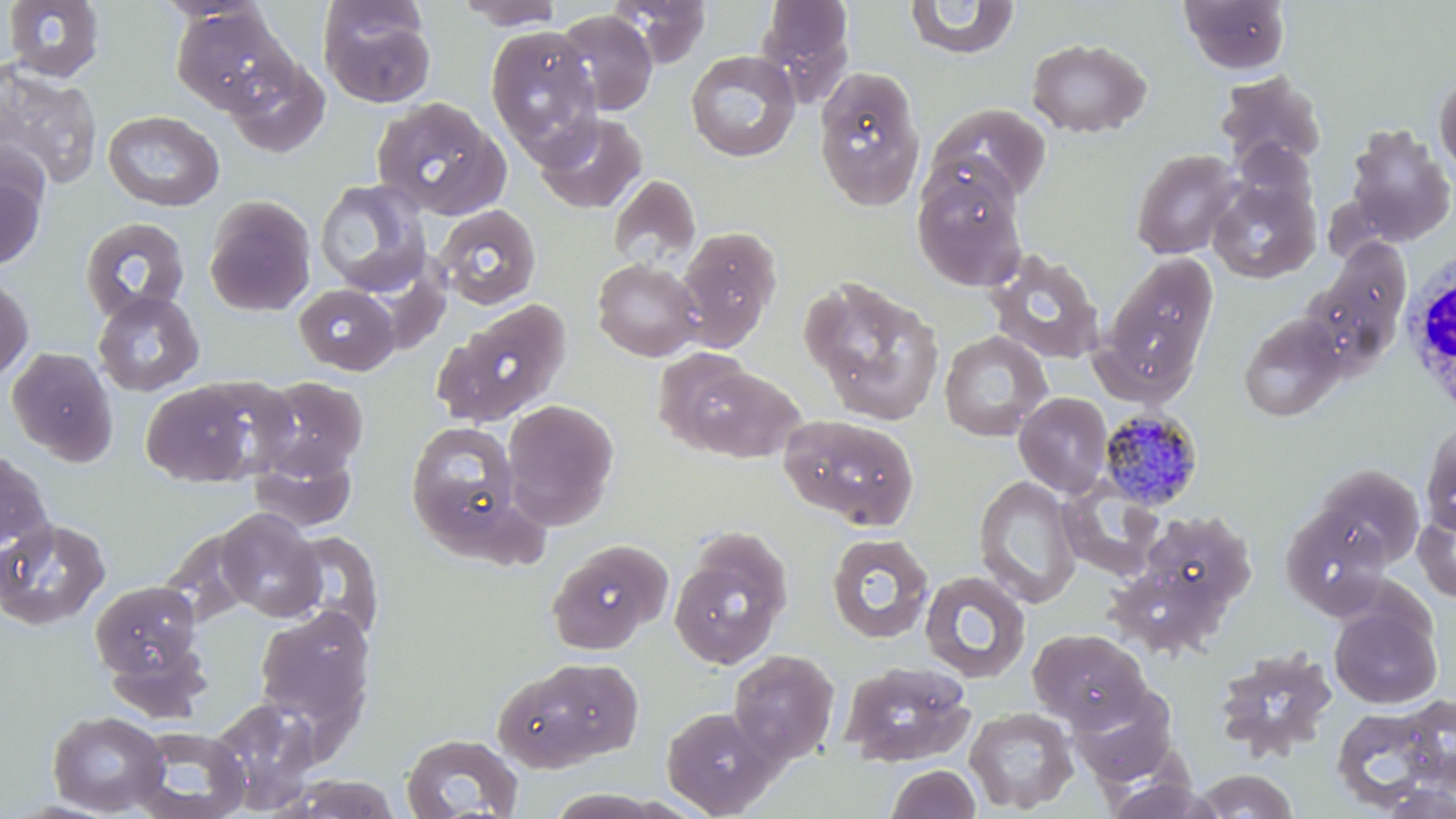
slide-level diagnosis = Plasmodium malariae
stain = May-Grünwald-Giemsa
uninfected red blood cell locations = approximate bounding boxes as named x1/y1/x2/y2 corners in pixels: (x1=2, y1=0, x2=106, y2=83), (x1=451, y1=0, x2=567, y2=29), (x1=606, y1=0, x2=712, y2=68), (x1=755, y1=0, x2=854, y2=90), (x1=1178, y1=0, x2=1292, y2=76), (x1=904, y1=1, x2=1020, y2=59), (x1=317, y1=2, x2=437, y2=109), (x1=170, y1=5, x2=298, y2=117), (x1=555, y1=10, x2=659, y2=116), (x1=484, y1=25, x2=602, y2=156), (x1=1026, y1=37, x2=1151, y2=138), (x1=685, y1=50, x2=801, y2=163), (x1=222, y1=52, x2=329, y2=159), (x1=0, y1=58, x2=103, y2=193), (x1=814, y1=67, x2=926, y2=211), (x1=1434, y1=68, x2=1456, y2=179), (x1=1215, y1=71, x2=1327, y2=172), (x1=371, y1=97, x2=511, y2=219), (x1=928, y1=103, x2=1051, y2=204), (x1=102, y1=110, x2=225, y2=211), (x1=534, y1=111, x2=648, y2=214), (x1=1342, y1=124, x2=1456, y2=247), (x1=1230, y1=138, x2=1319, y2=218), (x1=1130, y1=148, x2=1242, y2=259), (x1=911, y1=162, x2=1028, y2=291), (x1=0, y1=163, x2=47, y2=272), (x1=607, y1=173, x2=702, y2=271), (x1=1207, y1=177, x2=1321, y2=283), (x1=313, y1=178, x2=432, y2=298), (x1=203, y1=195, x2=316, y2=316), (x1=433, y1=204, x2=542, y2=310), (x1=79, y1=216, x2=190, y2=323), (x1=674, y1=226, x2=782, y2=350), (x1=1305, y1=239, x2=1412, y2=371), (x1=983, y1=249, x2=1106, y2=365), (x1=1099, y1=255, x2=1219, y2=396), (x1=592, y1=258, x2=703, y2=361), (x1=0, y1=275, x2=34, y2=384), (x1=800, y1=275, x2=945, y2=425), (x1=293, y1=282, x2=400, y2=375), (x1=92, y1=289, x2=205, y2=396), (x1=433, y1=298, x2=573, y2=427), (x1=1238, y1=313, x2=1346, y2=422), (x1=939, y1=330, x2=1052, y2=441), (x1=6, y1=347, x2=119, y2=467), (x1=663, y1=357, x2=804, y2=464), (x1=188, y1=376, x2=303, y2=477), (x1=254, y1=376, x2=368, y2=479), (x1=140, y1=380, x2=263, y2=487), (x1=1014, y1=392, x2=1113, y2=498), (x1=501, y1=398, x2=619, y2=526), (x1=778, y1=413, x2=921, y2=528), (x1=407, y1=420, x2=524, y2=546), (x1=1421, y1=422, x2=1456, y2=537), (x1=249, y1=446, x2=357, y2=532), (x1=1, y1=448, x2=55, y2=563), (x1=1311, y1=464, x2=1425, y2=570), (x1=974, y1=474, x2=1082, y2=608), (x1=1057, y1=481, x2=1165, y2=581), (x1=1414, y1=505, x2=1456, y2=603), (x1=1280, y1=506, x2=1391, y2=619), (x1=216, y1=508, x2=325, y2=622), (x1=1137, y1=509, x2=1256, y2=614), (x1=0, y1=519, x2=111, y2=630), (x1=282, y1=531, x2=383, y2=638), (x1=668, y1=532, x2=793, y2=671), (x1=826, y1=532, x2=934, y2=643), (x1=546, y1=539, x2=673, y2=655), (x1=919, y1=570, x2=1032, y2=683), (x1=90, y1=580, x2=203, y2=684), (x1=1329, y1=603, x2=1441, y2=709), (x1=254, y1=606, x2=376, y2=739), (x1=1028, y1=628, x2=1150, y2=730), (x1=1212, y1=647, x2=1339, y2=761), (x1=727, y1=649, x2=839, y2=765), (x1=494, y1=658, x2=641, y2=772), (x1=838, y1=661, x2=975, y2=767), (x1=1068, y1=683, x2=1180, y2=787), (x1=207, y1=699, x2=321, y2=814), (x1=1330, y1=703, x2=1451, y2=812), (x1=661, y1=706, x2=779, y2=817), (x1=965, y1=707, x2=1079, y2=814), (x1=47, y1=710, x2=169, y2=815), (x1=127, y1=725, x2=251, y2=819), (x1=400, y1=732, x2=524, y2=817), (x1=885, y1=764, x2=981, y2=819), (x1=1192, y1=769, x2=1300, y2=818), (x1=280, y1=774, x2=403, y2=818), (x1=1376, y1=780, x2=1455, y2=819)
white blood cell locations = approximate bounding boxes as named x1/y1/x2/y2 corners in pixels: (x1=1399, y1=247, x2=1455, y2=425)
magnification = 1000x
image size = 1456×819 pixels
preparation = thin blood film
field of view = one of a larger specimen
Plasmodium malariae-infected red blood cell locations = approximate bounding boxes as named x1/y1/x2/y2 corners in pixels: (x1=1098, y1=407, x2=1204, y2=511)
modality = light microscopy